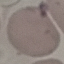

malaria_status: uninfected
capture: smartphone through the microscope eyepiece
preparation: thin smear
image_type: automatically extracted cell patch, resized to 64 × 64 pixels
stain: Giemsa